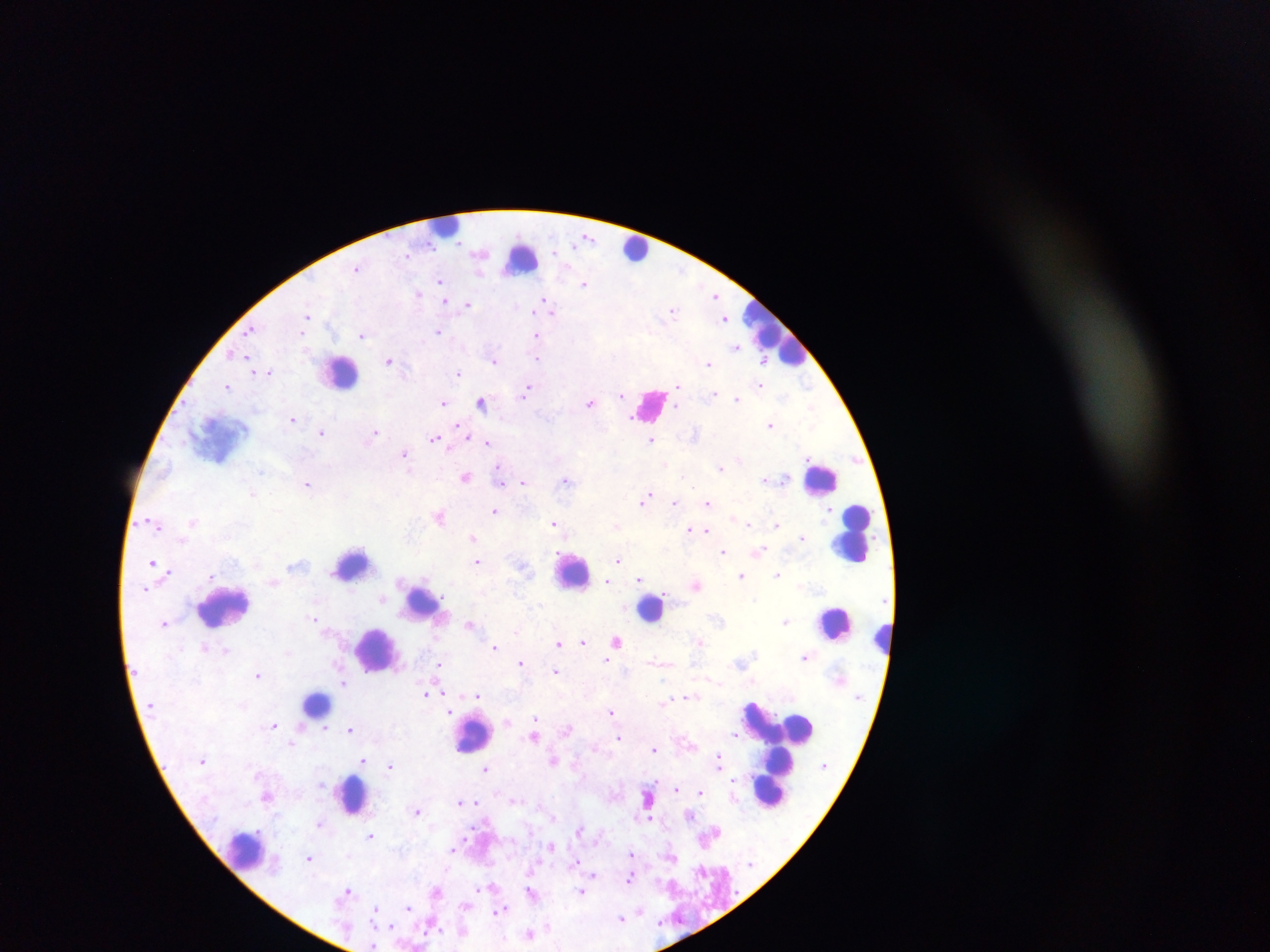
Approximate centers as (x, y) in pixels.
Summary:
  - Malaria parasite locations: (588, 236), (554, 252), (480, 254), (406, 255), (356, 268), (681, 270), (439, 280), (585, 284), (419, 294), (715, 295), (544, 298), (445, 300), (468, 304), (517, 306), (552, 313), (673, 313), (308, 316), (724, 319), (252, 330), (437, 332), (362, 335), (536, 336), (737, 346), (232, 354), (538, 359), (493, 360), (389, 361), (764, 361), (708, 363), (268, 371), (459, 373), (806, 383), (760, 385), (228, 386), (678, 386), (526, 391), (621, 394), (713, 394), (737, 398), (590, 402), (444, 403), (482, 403), (676, 407), (811, 407), (293, 419), (770, 425), (460, 426), (321, 432), (375, 433), (464, 433), (695, 433), (435, 437), (651, 440), (487, 443), (405, 454), (739, 460), (665, 464), (721, 467), (260, 471), (500, 475), (466, 477), (784, 478), (566, 480), (764, 480), (523, 482), (308, 484), (253, 494), (645, 497), (675, 502), (707, 502), (494, 511), (439, 516), (192, 521), (554, 524), (748, 524), (777, 525), (616, 526), (689, 529), (703, 531), (802, 537), (473, 538), (760, 550), (723, 551), (618, 560), (153, 562), (476, 562), (523, 566), (211, 575), (778, 575), (742, 577), (639, 580), (607, 581), (696, 585), (382, 600), (314, 619), (785, 621), (165, 623), (469, 624), (516, 630), (617, 641), (699, 641), (583, 642), (558, 644), (205, 646), (494, 647), (226, 650), (805, 657), (607, 661), (521, 663), (659, 663), (438, 665), (556, 671), (257, 675), (711, 679), (343, 683), (426, 693), (442, 693), (478, 695), (686, 696), (665, 702), (447, 703), (611, 711), (448, 712), (535, 718), (507, 722), (274, 725), (350, 728), (324, 729), (568, 730), (735, 734), (534, 736), (619, 737), (292, 743), (654, 749), (362, 760), (553, 761), (718, 761), (390, 765), (486, 769), (678, 789), (700, 791), (267, 796), (515, 799), (461, 802), (476, 802), (417, 811), (691, 815), (554, 817), (650, 819), (319, 823), (579, 829), (371, 836), (552, 845), (452, 851), (632, 853), (671, 856), (309, 858), (575, 863), (594, 875), (630, 877), (347, 889), (436, 891), (531, 891), (581, 892), (407, 907), (376, 910), (500, 911), (641, 911), (621, 918), (390, 924), (548, 926), (530, 933), (372, 946)
  - Leukocyte locations (subset; some below the resolvable size): (447, 225), (636, 248), (522, 258), (776, 332), (340, 371), (651, 404), (821, 479), (853, 533), (353, 565), (572, 572), (421, 604), (223, 607), (651, 608), (835, 622), (882, 639), (376, 649), (316, 702), (785, 727), (473, 734), (775, 780), (353, 794), (244, 850)
  - Field of view: single
  - Preparation: thick blood smear
  - Image size: 1270×952 pixels
  - Country: Ghana
  - Capture: mobile-phone photograph through a microscope